Describe the morphology of the red blood cells.
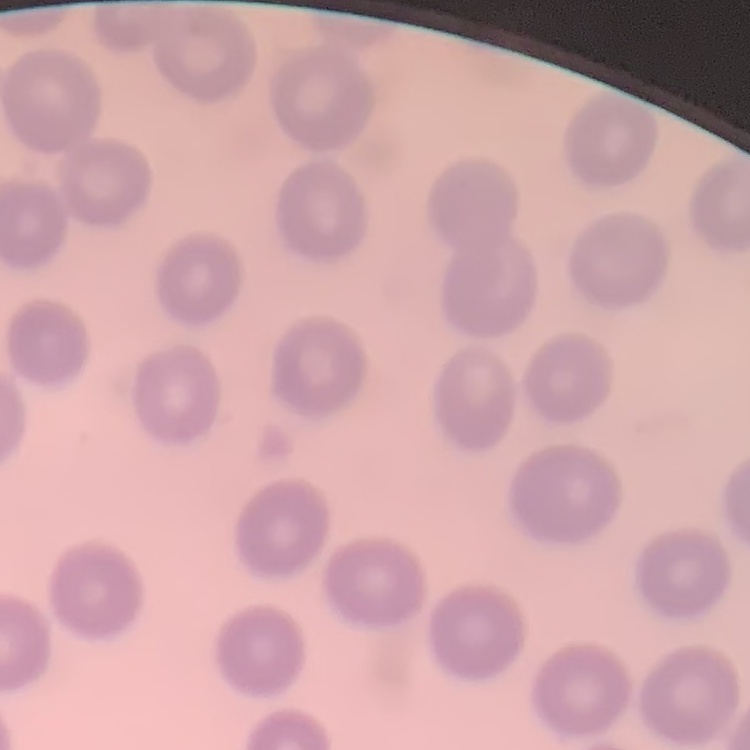
They show no rouleaux formation.

Thin blood film. Field's or Giemsa stain. One tile cut from a larger photomicrograph.